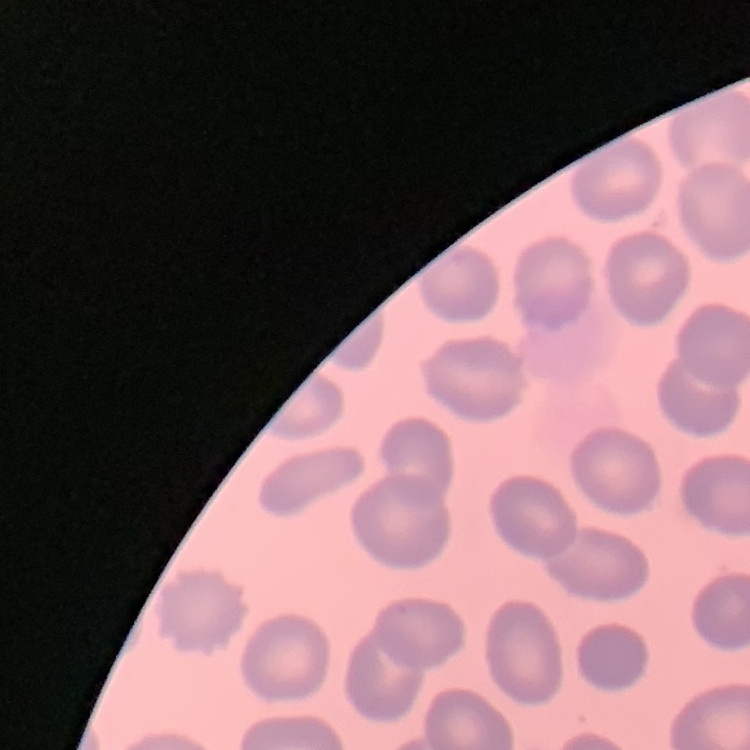
Summary:
  - Erythrocyte morphology: no rouleaux formation
  - Image type: one tile cut from a larger photomicrograph
  - Preparation: thin peripheral smear
  - Stain: Field's or Giemsa